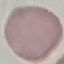

{
  "result": "no malaria parasites detected",
  "capture": "smartphone through the microscope eyepiece",
  "stain": "Giemsa",
  "preparation": "thin smear",
  "image_type": "automatically extracted cell patch, resized to 64 × 64 pixels"
}